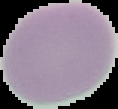
image_size: 118×109 pixels
image_type: cell region segmented out of the field of view; surrounding area masked to black
preparation: thin blood smear
result: negative for Plasmodium parasites